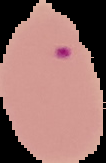

Summary:
  - Malaria status: parasitized
  - Image type: cell region segmented out of the field of view; surrounding area masked to black
  - Preparation: thin blood film
  - Image size: 106×163 pixels